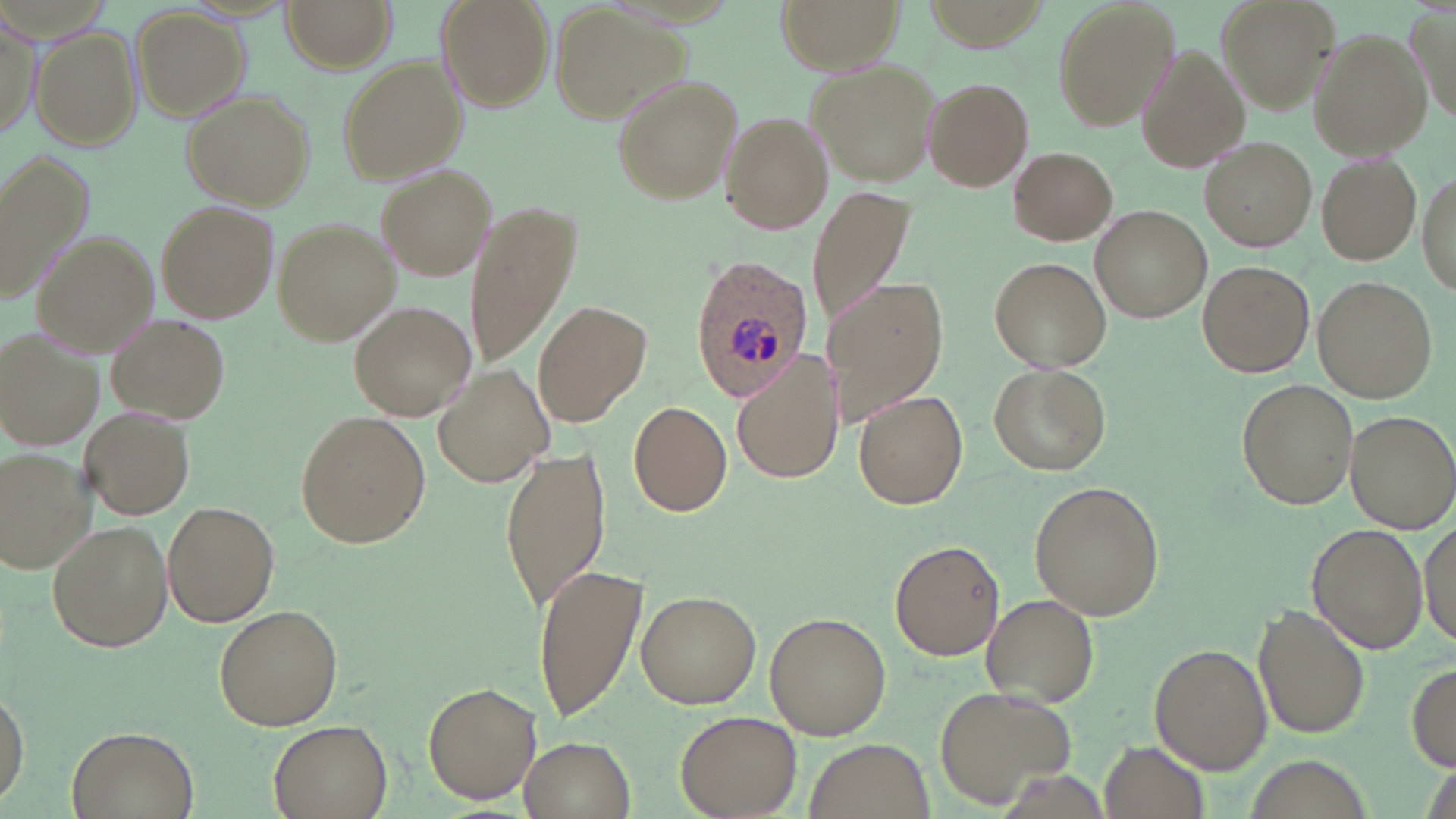

Summary:
  - Coordinate format: approximate bounding boxes as [x1, y1, x2, y2] in pixels
  - Uninfected red blood cell locations: [282, 0, 395, 71], [436, 0, 554, 111], [773, 0, 907, 74], [1049, 0, 1179, 134], [1214, 0, 1337, 111], [551, 6, 683, 120], [133, 9, 246, 119], [1413, 9, 1454, 122], [1, 12, 41, 147], [34, 27, 140, 152], [1311, 31, 1430, 157], [1135, 44, 1246, 173], [337, 56, 464, 184], [807, 59, 941, 186], [610, 77, 742, 205], [924, 78, 1033, 190], [182, 90, 312, 208], [720, 111, 828, 235], [1201, 137, 1316, 252], [1007, 147, 1117, 245], [2, 154, 95, 306], [1318, 155, 1423, 263], [377, 164, 497, 281], [1417, 174, 1455, 297], [808, 185, 918, 329], [157, 200, 278, 323], [466, 204, 583, 362], [1092, 207, 1210, 322], [272, 218, 399, 346], [35, 232, 159, 355], [989, 256, 1111, 371], [1199, 261, 1313, 376], [1314, 277, 1437, 402], [826, 281, 947, 424], [349, 300, 478, 421], [536, 300, 649, 425], [108, 316, 230, 424], [0, 330, 97, 448], [730, 351, 844, 487], [435, 363, 552, 490], [990, 363, 1111, 476], [1238, 380, 1358, 508], [854, 390, 969, 509], [629, 400, 733, 516], [79, 406, 194, 519], [1345, 409, 1456, 536], [298, 412, 430, 547], [500, 445, 612, 613], [0, 448, 93, 571], [1029, 481, 1166, 620], [162, 501, 280, 625], [1417, 518, 1455, 644], [45, 520, 173, 654], [1307, 524, 1428, 654], [888, 538, 1007, 662], [532, 563, 648, 722], [637, 590, 761, 709], [983, 593, 1098, 705], [215, 604, 343, 730], [1255, 604, 1371, 738], [766, 612, 890, 739], [1149, 644, 1271, 772], [1407, 660, 1456, 773], [423, 682, 540, 805], [1, 684, 28, 805], [935, 686, 1074, 807], [674, 708, 801, 817], [267, 720, 392, 818], [66, 725, 201, 819], [520, 734, 635, 819], [803, 737, 935, 819], [1102, 738, 1209, 818], [1242, 754, 1372, 819]
  - Plasmodium ovale-infected red blood cell locations: [691, 253, 812, 397]
  - Slide-level diagnosis: Plasmodium ovale
  - Magnification: 1000x
  - Modality: light microscopy
  - Field of view: one of a larger specimen
  - Stain: May-Grünwald-Giemsa
  - Image size: 1456×819 pixels
  - Preparation: thin blood film